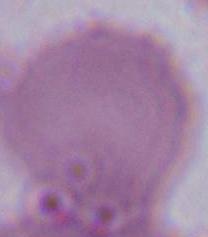

Summary:
  - Identification: red blood cell
  - Magnification: 1000x
  - Modality: photomicrograph